Classify this cell by malaria status.
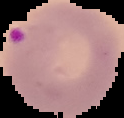
Parasitized.

Cell region segmented out of the field of view; the surrounding area is masked to black. From a thin blood smear. Image is 124×118 pixels.